Name the parasite shown.
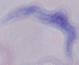

A trypanosome.

modality = micrograph
magnification = 1000x